Report the malaria status of this cell.
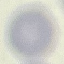

Uninfected.

Giemsa-stained preparation. Acquired by smartphone through the microscope eyepiece. Thin smear of blood. Automatically extracted cell patch, resized to 64 × 64 pixels.